Give the extent of all uninfected red blood cells.
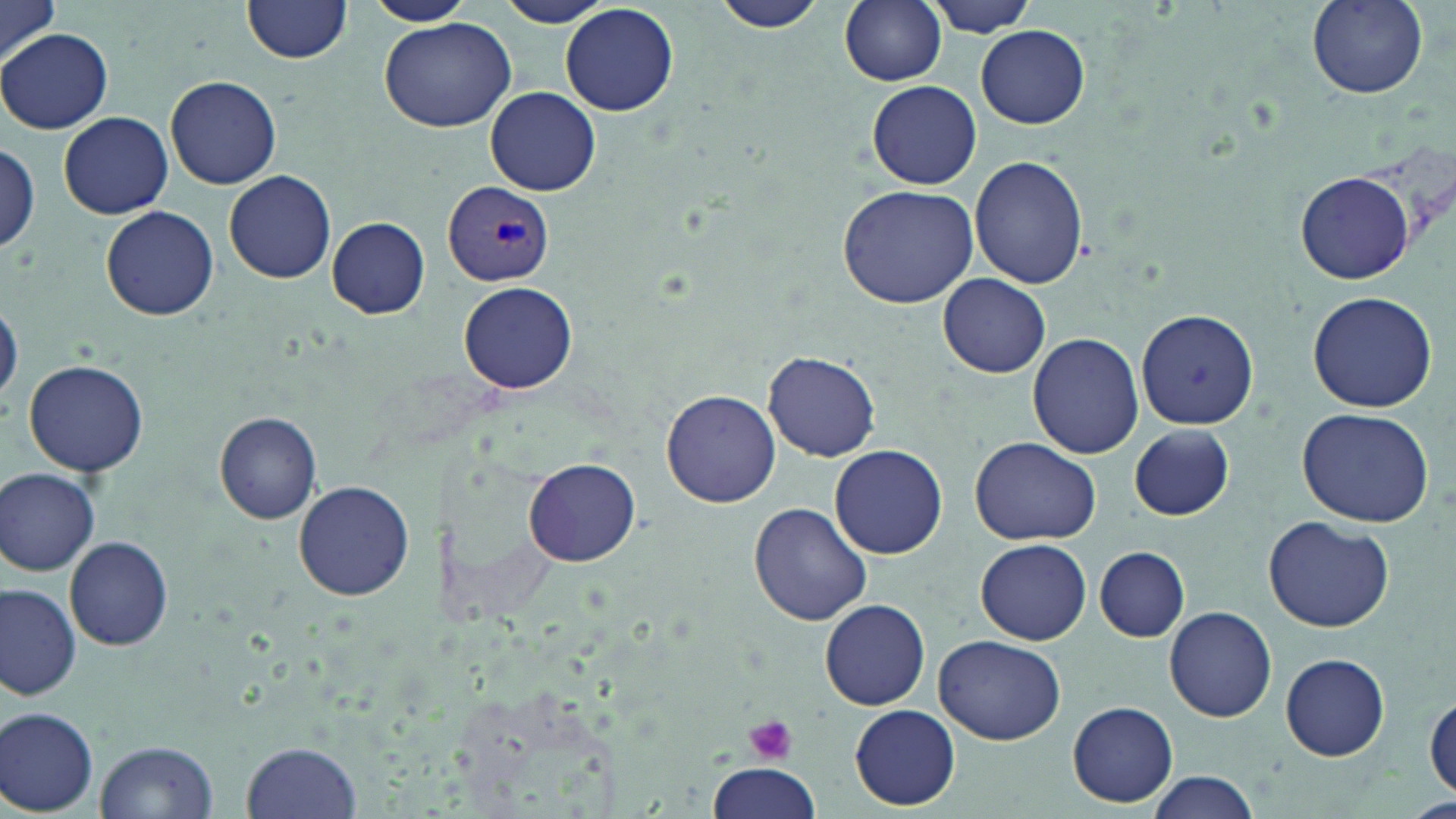
Approximate bounding boxes as [x1, y1, x2, y2] in pixels.
Uninfected red blood cells: [1, 0, 61, 67], [366, 0, 473, 25], [498, 0, 613, 28], [712, 0, 833, 36], [839, 0, 947, 86], [921, 0, 1042, 36], [1307, 1, 1428, 98], [241, 2, 354, 66], [560, 3, 679, 117], [378, 18, 516, 131], [976, 26, 1090, 128], [2, 29, 113, 135], [165, 74, 282, 188], [867, 79, 982, 189], [486, 87, 600, 197], [58, 111, 173, 219], [0, 144, 41, 253], [969, 154, 1088, 287], [224, 170, 336, 284], [1296, 171, 1414, 283], [836, 184, 981, 309], [101, 206, 219, 321], [326, 217, 430, 318], [939, 275, 1050, 378], [459, 282, 579, 394], [1307, 290, 1440, 413], [0, 302, 22, 405], [1135, 308, 1259, 428], [1027, 333, 1144, 461], [763, 352, 881, 461], [23, 358, 149, 476], [662, 390, 779, 508], [1297, 407, 1433, 528], [214, 411, 323, 524], [1130, 424, 1234, 519], [969, 436, 1099, 545], [829, 444, 947, 559], [523, 458, 641, 567], [1, 468, 100, 576], [293, 481, 417, 602], [748, 501, 873, 627], [1264, 515, 1394, 633], [65, 535, 173, 651], [976, 538, 1092, 645], [1094, 547, 1189, 641], [0, 582, 80, 700], [818, 599, 931, 711], [1165, 607, 1277, 722], [935, 634, 1065, 746], [1280, 653, 1390, 759], [1426, 696, 1456, 798], [1069, 701, 1179, 806], [850, 705, 960, 810], [1, 707, 100, 815], [241, 740, 362, 818], [95, 741, 217, 818], [707, 761, 821, 819], [1146, 772, 1262, 818], [1411, 798, 1456, 819].

slide-level diagnosis = Plasmodium vivax
modality = light microscopy
Plasmodium vivax-infected red blood cell locations = approximate bounding boxes as [x1, y1, x2, y2] in pixels: [443, 182, 555, 287]
preparation = thin blood smear
field of view = one of a larger specimen
magnification = 1000x
image size = 1456×819 pixels
platelet locations = approximate bounding boxes as [x1, y1, x2, y2] in pixels: [745, 716, 798, 765]
stain = May-Grünwald-Giemsa